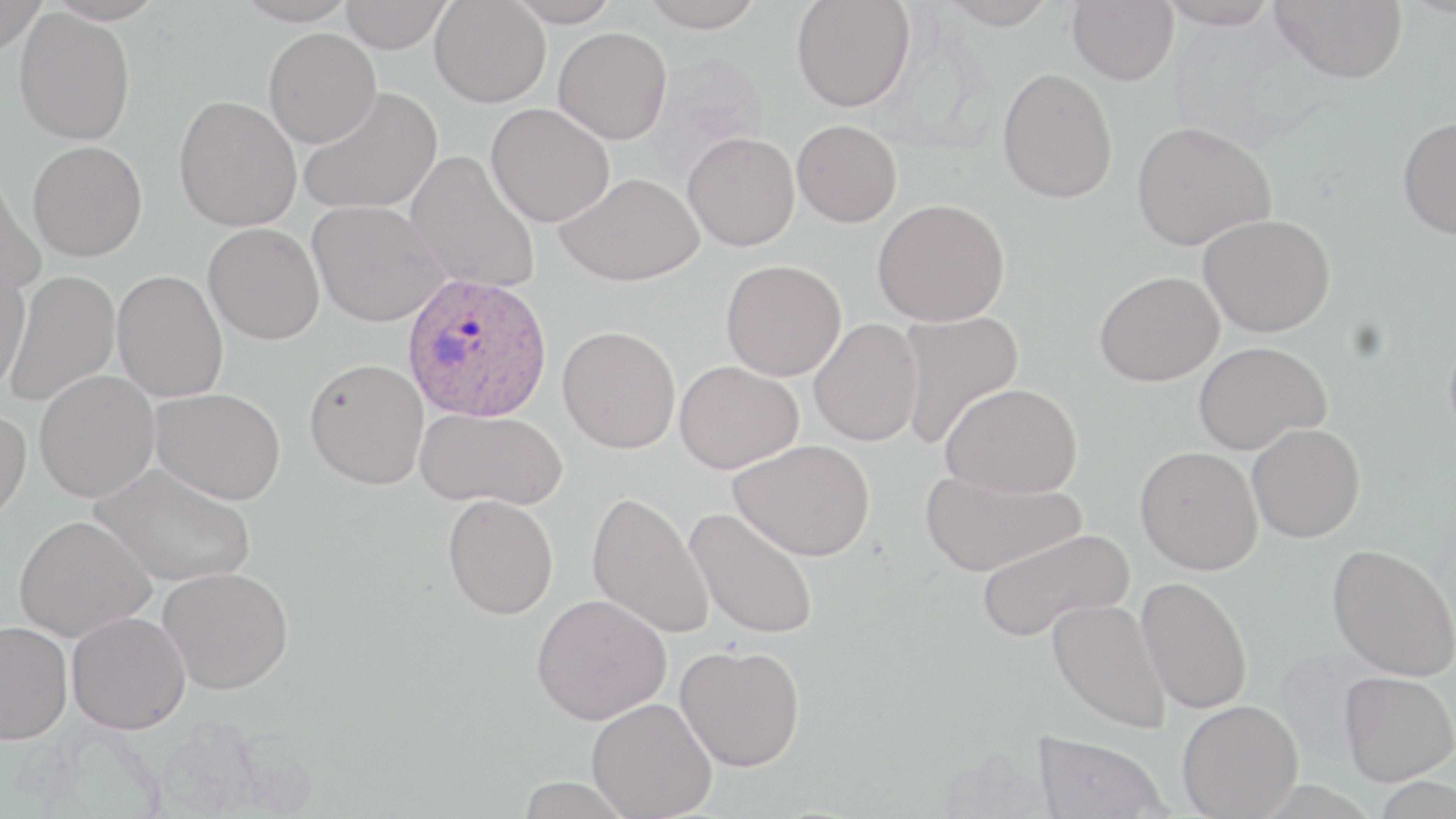
Approximate bounding boxes as named x1/y1/x2/y2 corners in pixels. Plasmodium ovale-infected red blood cell locations: (x1=401, y1=273, x2=553, y2=423). Uninfected red blood cell locations: (x1=0, y1=0, x2=48, y2=55), (x1=232, y1=0, x2=358, y2=26), (x1=340, y1=0, x2=452, y2=53), (x1=507, y1=0, x2=621, y2=27), (x1=640, y1=0, x2=766, y2=31), (x1=791, y1=0, x2=915, y2=112), (x1=938, y1=0, x2=1058, y2=29), (x1=1067, y1=0, x2=1179, y2=85), (x1=1156, y1=0, x2=1283, y2=29), (x1=1271, y1=0, x2=1408, y2=84), (x1=430, y1=1, x2=551, y2=107), (x1=14, y1=8, x2=135, y2=145), (x1=553, y1=27, x2=672, y2=144), (x1=264, y1=28, x2=382, y2=147), (x1=998, y1=67, x2=1118, y2=203), (x1=297, y1=86, x2=442, y2=215), (x1=174, y1=95, x2=301, y2=231), (x1=485, y1=103, x2=614, y2=227), (x1=1396, y1=115, x2=1456, y2=239), (x1=792, y1=119, x2=902, y2=227), (x1=1132, y1=120, x2=1277, y2=250), (x1=683, y1=132, x2=800, y2=251), (x1=27, y1=141, x2=147, y2=261), (x1=405, y1=150, x2=541, y2=294), (x1=0, y1=168, x2=47, y2=297), (x1=557, y1=172, x2=705, y2=285), (x1=873, y1=199, x2=1009, y2=327), (x1=308, y1=200, x2=450, y2=326), (x1=1199, y1=213, x2=1335, y2=336), (x1=203, y1=222, x2=324, y2=344), (x1=721, y1=260, x2=846, y2=381), (x1=0, y1=262, x2=32, y2=396), (x1=4, y1=270, x2=119, y2=409), (x1=112, y1=270, x2=229, y2=403), (x1=1095, y1=270, x2=1224, y2=386), (x1=896, y1=310, x2=1024, y2=449), (x1=809, y1=318, x2=923, y2=446), (x1=557, y1=325, x2=681, y2=453), (x1=1443, y1=326, x2=1456, y2=448), (x1=1193, y1=341, x2=1331, y2=454), (x1=304, y1=358, x2=429, y2=489), (x1=674, y1=360, x2=803, y2=474), (x1=34, y1=370, x2=159, y2=502), (x1=940, y1=382, x2=1083, y2=498), (x1=150, y1=387, x2=286, y2=505), (x1=415, y1=407, x2=568, y2=511), (x1=0, y1=408, x2=32, y2=529), (x1=1247, y1=423, x2=1365, y2=543), (x1=730, y1=439, x2=875, y2=560), (x1=1135, y1=445, x2=1263, y2=574), (x1=89, y1=461, x2=256, y2=588), (x1=920, y1=468, x2=1085, y2=577), (x1=586, y1=491, x2=714, y2=640), (x1=443, y1=494, x2=558, y2=619), (x1=683, y1=506, x2=820, y2=640), (x1=13, y1=514, x2=155, y2=642), (x1=975, y1=527, x2=1134, y2=643), (x1=1327, y1=543, x2=1456, y2=681), (x1=158, y1=566, x2=294, y2=695), (x1=1136, y1=576, x2=1253, y2=714), (x1=531, y1=594, x2=671, y2=724), (x1=1047, y1=598, x2=1172, y2=733), (x1=66, y1=611, x2=191, y2=734), (x1=0, y1=620, x2=73, y2=743), (x1=675, y1=644, x2=805, y2=771), (x1=1340, y1=671, x2=1456, y2=785), (x1=587, y1=697, x2=717, y2=819), (x1=1177, y1=700, x2=1303, y2=818), (x1=1032, y1=731, x2=1170, y2=819), (x1=1369, y1=775, x2=1456, y2=818), (x1=515, y1=776, x2=638, y2=819). Slide-level diagnosis: Plasmodium ovale. Captured at 1000x magnification. May-Grünwald-Giemsa stain. Thin blood smear. Single field of view. Image is 1456×819 pixels. Optical microscopy.